Locate every Plasmodium parasite.
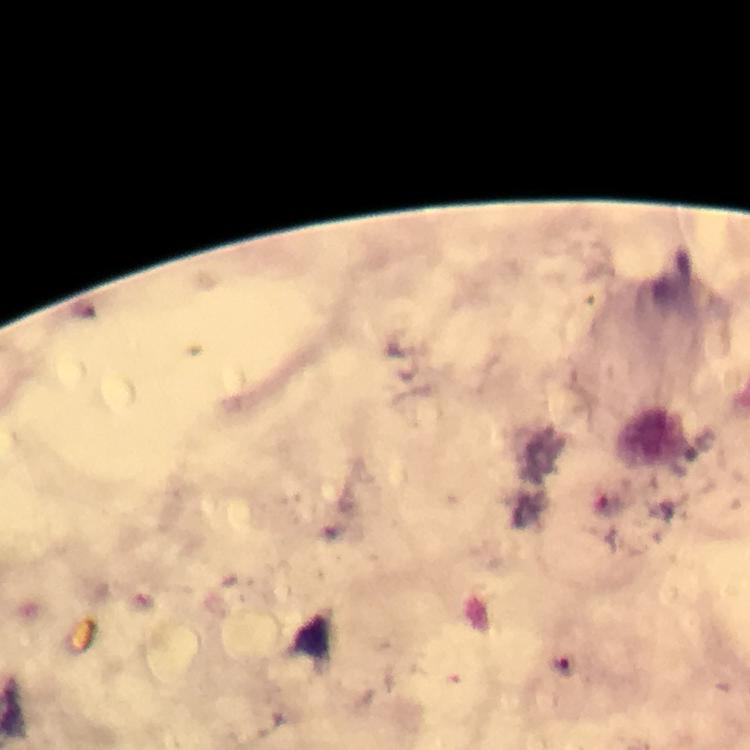

Approximate object centers, in pixels from the top-left corner.
Plasmodium parasites: (x=562, y=666).

100x magnification. A crop from one field of view. Immersion oil was used. Smartphone photograph taken through a microscope. Thick smear. From a diagnostic examination for malaria. Giemsa stain. Image is 750×750 pixels.